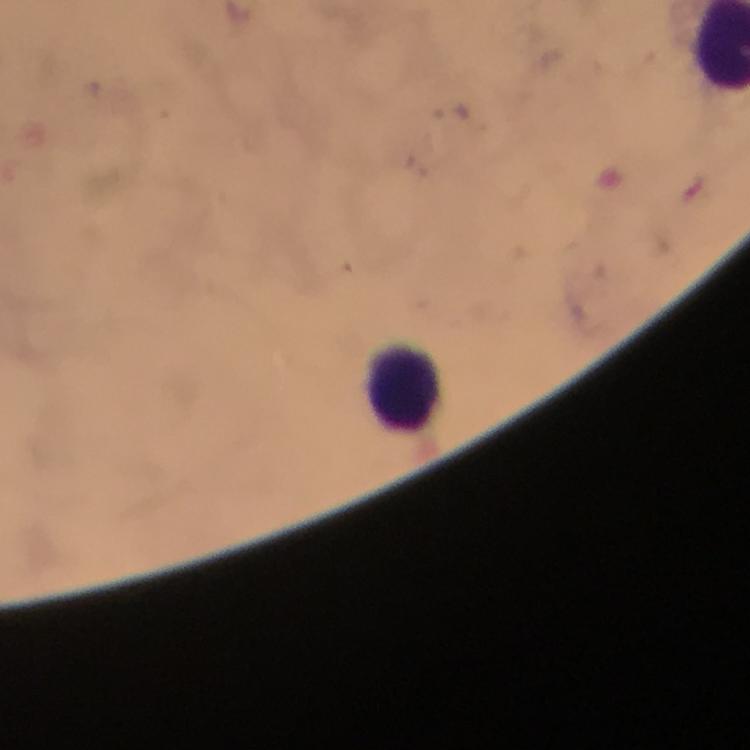

Approximate centers as {x, y} in pixels.
Summary:
  - Leukocyte locations: {406, 386}
  - Immersion oil: used
  - Context: from a diagnostic examination for malaria
  - Image size: 750×750 pixels
  - Plasmodium parasites: none seen
  - Cropped from: a single field of view
  - Stain: Giemsa
  - Capture: smartphone camera through the microscope
  - Magnification: 100x
  - Preparation: thick blood smear